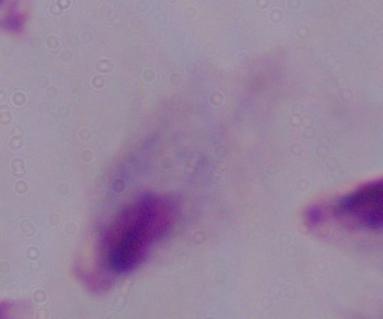

Summary:
  - Magnification: 1000x
  - Identification: trichomonad
  - Modality: micrograph